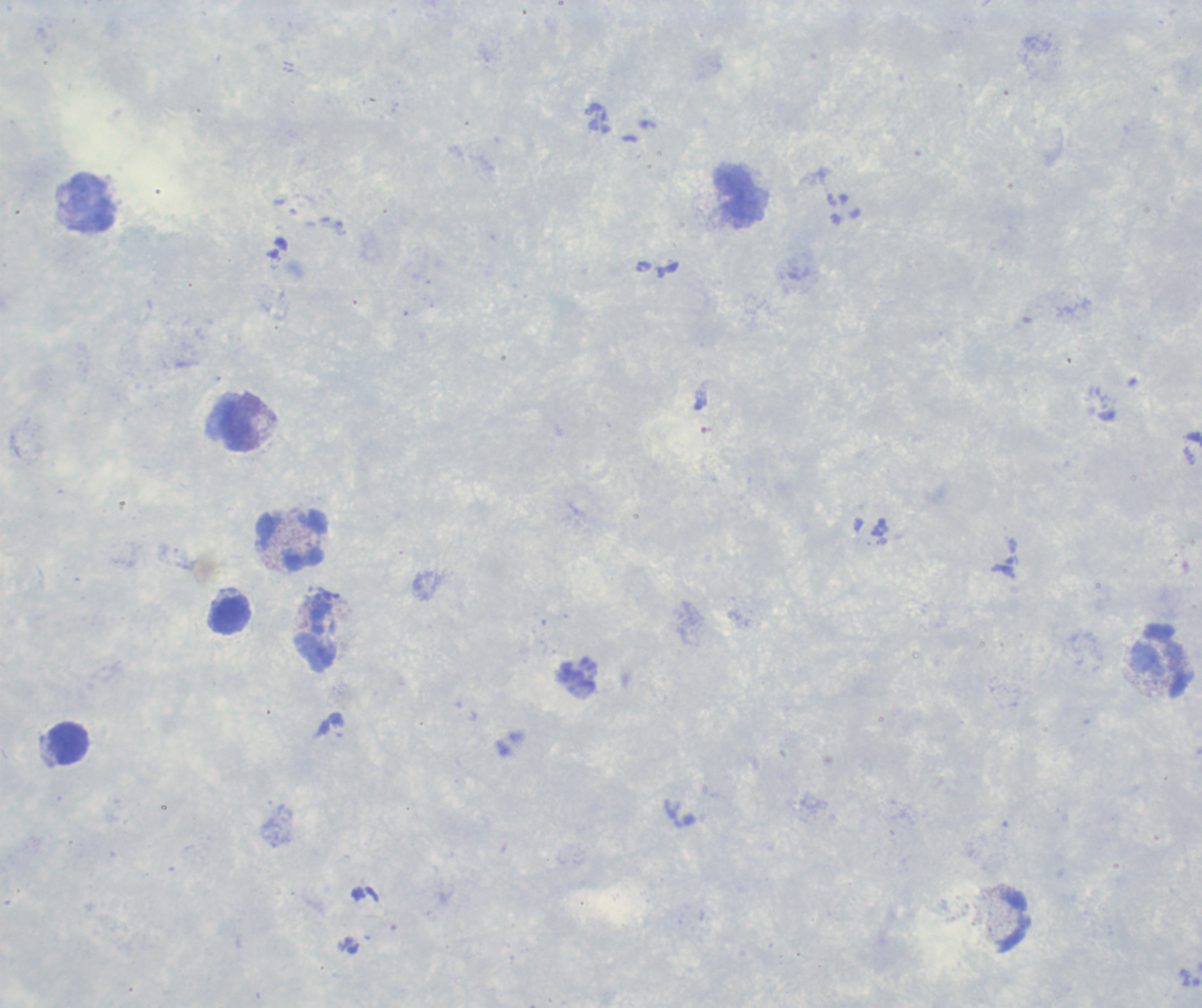
{
  "stain": "Romanowsky",
  "field_of_view": "single",
  "background_quality": "unsatisfactory",
  "image_size": "1202×1008 pixels",
  "leukocyte_locations": "approximate centers as {x, y} in pixels: {741, 197}, {91, 204}, {236, 425}, {293, 540}, {230, 614}, {316, 636}, {1163, 662}, {68, 744}",
  "context": "previously used in a real diagnosis",
  "result": "no malaria parasites seen",
  "preparation": "thick blood film",
  "coloration_quality": "good",
  "magnification": "100x"
}